Give the position of every Plasmodium parasite visible.
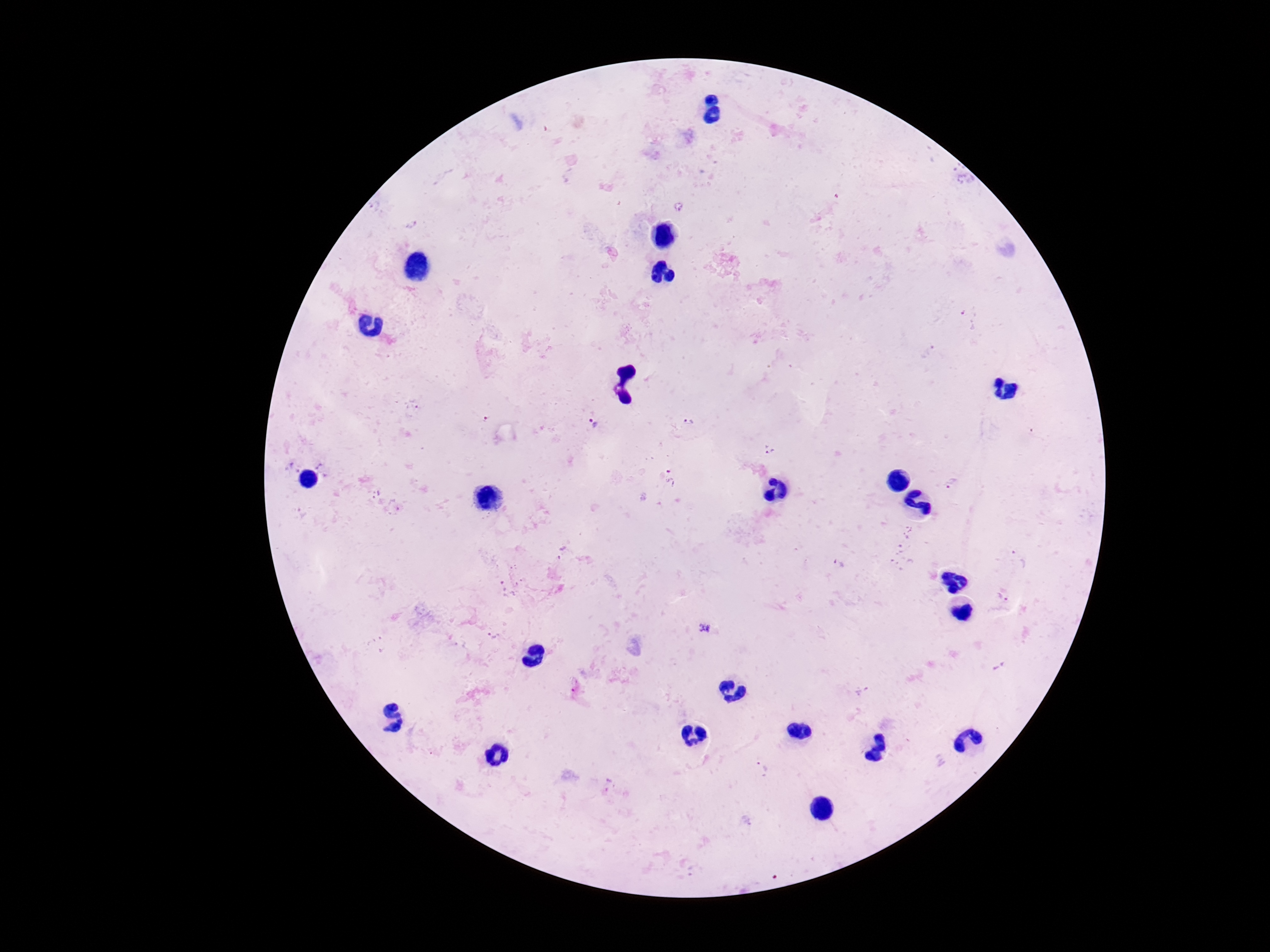

Approximate centers as [x, y] in pixels.
Plasmodium parasites: [689, 422], [592, 424], [768, 449], [672, 477], [952, 483], [1003, 597], [704, 627], [763, 768], [609, 786].

{
  "field_of_view": "single",
  "patient_malaria_status": "infected",
  "preparation": "thick blood smear",
  "magnification": "100x",
  "capture": "smartphone camera through the microscope eyepiece",
  "image_size": "1270×952 pixels",
  "stain": "Giemsa"
}